State which parasite is depicted.
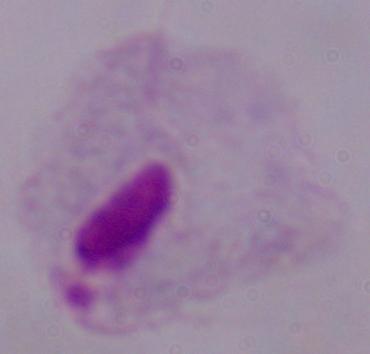

A trichomonad.

Summary:
  - Magnification: 1000x
  - Modality: micrograph